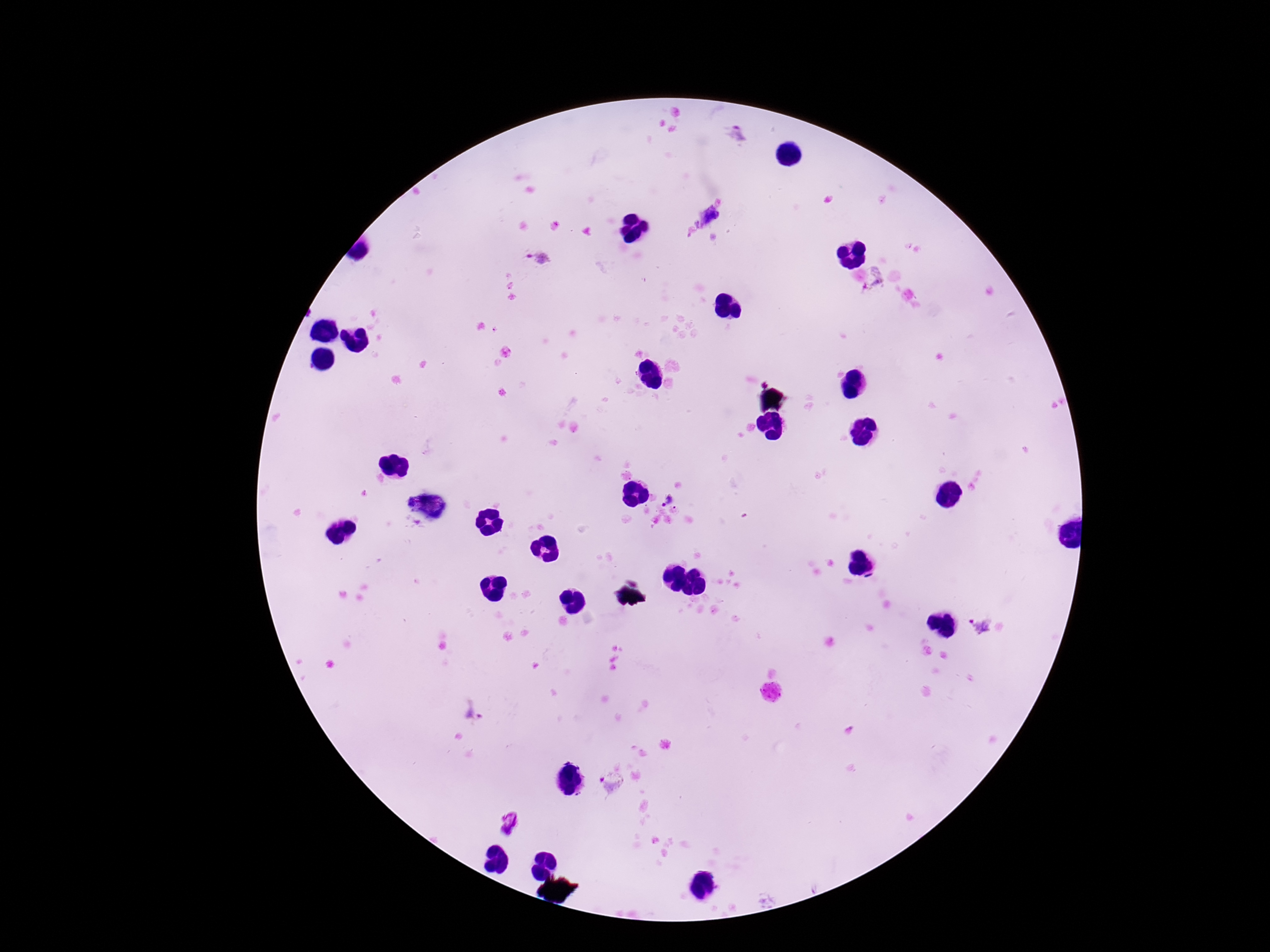

capture = smartphone camera through the microscope eyepiece
stain = Giemsa
field of view = one from this slide
Plasmodium parasite locations = approximate centers as (x, y) in pixels: (737, 133), (710, 217), (538, 258), (875, 279), (668, 501), (981, 626), (612, 783), (513, 823)
image size = 1270×952 pixels
magnification = 100x
preparation = thick blood smear
patient malaria status = infected